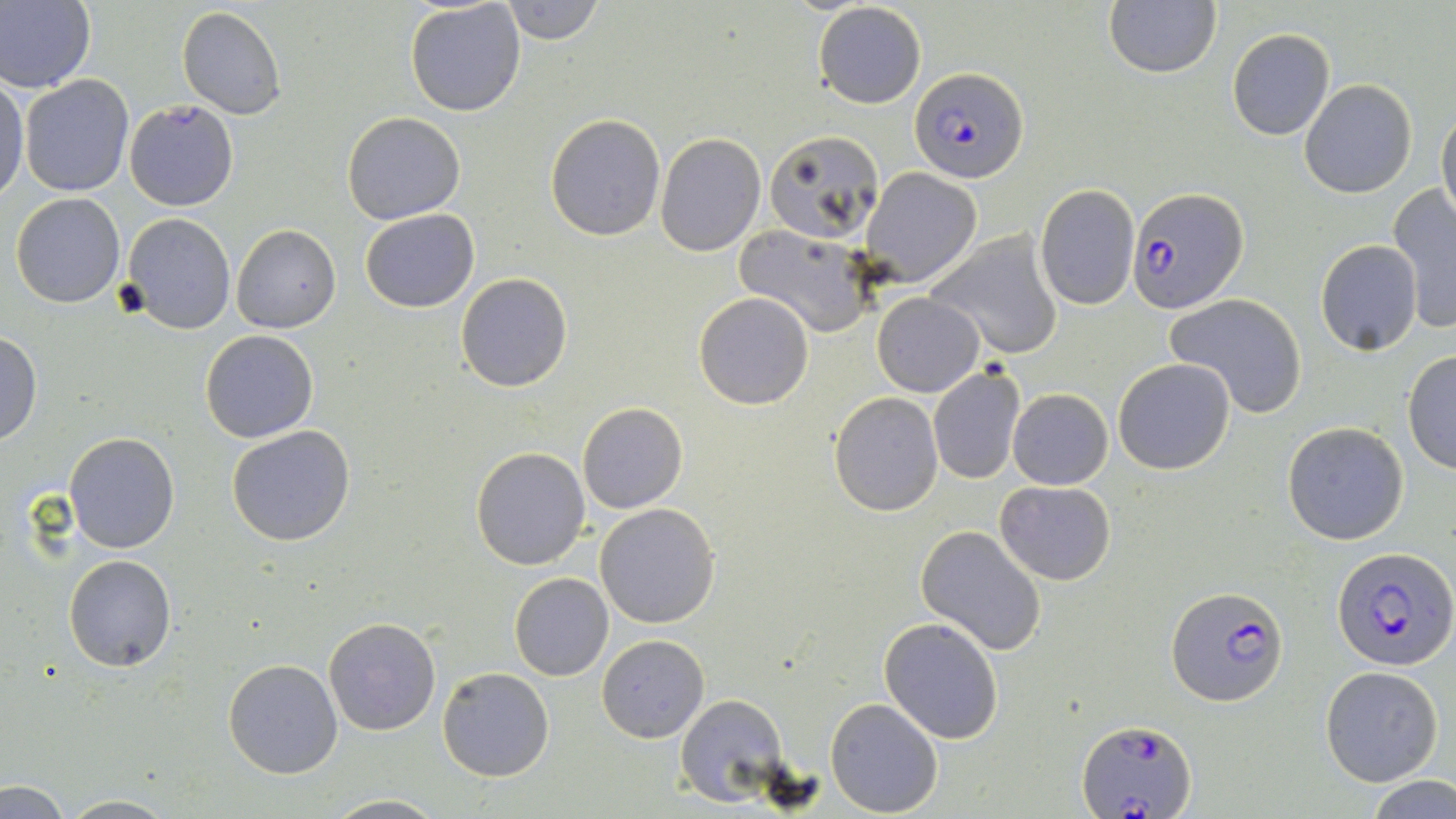
slide_level_diagnosis: Plasmodium falciparum
field_of_view: one of a larger specimen
magnification: 1000x
stain: May-Grünwald-Giemsa
modality: light microscopy
plasmodium_falciparum_infected_red_blood_cell_locations: 'approximate bounding boxes as (x1,y1)-(x2,y2) corner pairs in pixels: (912,68)-(1026,184), (1127,188)-(1246,315), (1332,547)-(1453,673), (1168,585)-(1288,706), (1078,717)-(1198,817)'
uninfected_red_blood_cell_locations: 'approximate bounding boxes as (x1,y1)-(x2,y2) corner pairs in pixels: (0,0)-(96,95), (405,1)-(526,117), (497,1)-(607,46), (812,1)-(927,110), (1103,1)-(1221,80), (176,6)-(287,120), (1226,29)-(1335,141), (20,74)-(135,197), (0,75)-(28,202), (1299,80)-(1417,199), (124,100)-(240,211), (1437,107)-(1456,229), (341,111)-(467,225), (544,114)-(666,241), (764,130)-(885,245), (656,133)-(765,256), (859,167)-(982,287), (1034,182)-(1140,311), (1387,185)-(1456,335), (11,193)-(126,308), (359,209)-(480,314), (121,213)-(235,334), (232,224)-(342,333), (734,226)-(876,336), (927,231)-(1066,361), (1316,240)-(1423,355), (455,272)-(573,393), (693,291)-(815,410), (872,292)-(986,397), (1165,294)-(1309,419), (201,329)-(319,443), (0,330)-(42,446), (1402,350)-(1456,475), (1112,357)-(1236,476), (927,365)-(1025,485), (1008,388)-(1113,490), (829,392)-(942,515), (577,401)-(688,513), (1283,421)-(1409,545), (226,424)-(357,547), (64,431)-(180,553), (471,446)-(592,571), (993,480)-(1117,585), (594,502)-(721,629), (915,524)-(1047,656), (63,555)-(176,672), (509,573)-(614,681), (323,616)-(443,736), (879,616)-(1004,742), (596,634)-(709,741), (224,657)-(344,778), (1319,665)-(1444,786), (438,667)-(554,781), (676,694)-(791,809), (825,698)-(943,817), (1367,777)-(1456,819), (1,782)-(75,818), (56,794)-(183,818), (322,794)-(449,818)'
image_size: 1456×819 pixels
preparation: thin blood film